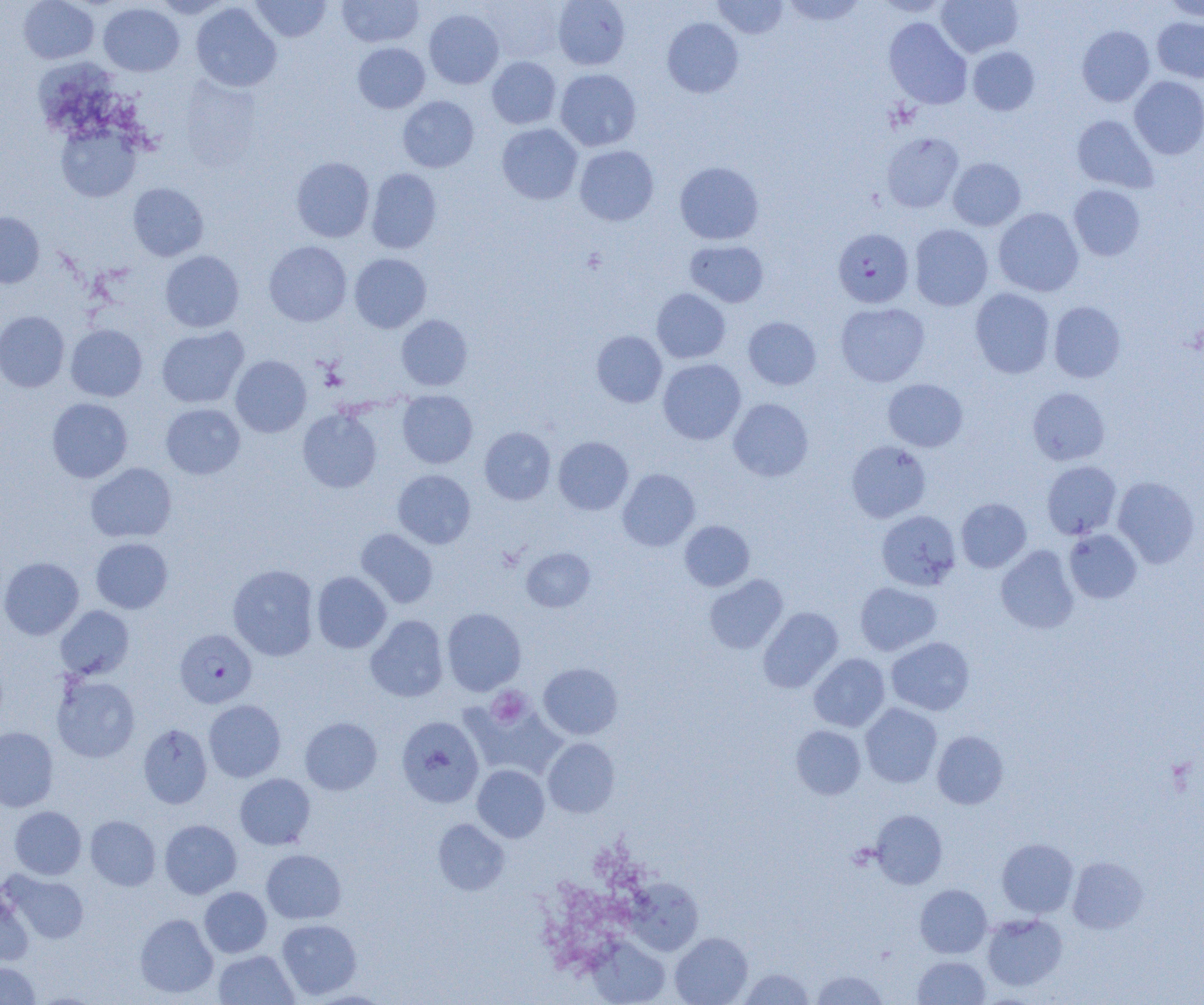

Summary:
  - Coordinate format: approximate bounding boxes as named x1/y1/x2/y2 corners in pixels
  - Platelet locations: (x1=487, y1=686, x2=531, y2=728)
  - Uninfected red blood cell locations: (x1=18, y1=0, x2=98, y2=63), (x1=152, y1=0, x2=231, y2=18), (x1=251, y1=0, x2=331, y2=42), (x1=337, y1=0, x2=424, y2=47), (x1=478, y1=0, x2=565, y2=64), (x1=553, y1=0, x2=630, y2=70), (x1=712, y1=0, x2=788, y2=39), (x1=779, y1=0, x2=868, y2=27), (x1=872, y1=0, x2=953, y2=18), (x1=936, y1=0, x2=1023, y2=57), (x1=1161, y1=0, x2=1204, y2=21), (x1=191, y1=2, x2=281, y2=92), (x1=99, y1=3, x2=184, y2=76), (x1=424, y1=9, x2=504, y2=89), (x1=1152, y1=16, x2=1204, y2=82), (x1=662, y1=17, x2=744, y2=98), (x1=884, y1=17, x2=972, y2=109), (x1=1077, y1=25, x2=1155, y2=107), (x1=353, y1=42, x2=430, y2=113), (x1=967, y1=46, x2=1040, y2=115), (x1=33, y1=56, x2=119, y2=132), (x1=487, y1=56, x2=561, y2=129), (x1=555, y1=69, x2=641, y2=151), (x1=1129, y1=76, x2=1204, y2=159), (x1=178, y1=77, x2=263, y2=172), (x1=398, y1=96, x2=479, y2=172), (x1=1071, y1=115, x2=1159, y2=193), (x1=496, y1=123, x2=583, y2=204), (x1=57, y1=125, x2=140, y2=202), (x1=881, y1=132, x2=964, y2=213), (x1=574, y1=145, x2=659, y2=226), (x1=291, y1=157, x2=374, y2=242), (x1=948, y1=158, x2=1025, y2=230), (x1=674, y1=161, x2=764, y2=245), (x1=366, y1=168, x2=441, y2=254), (x1=127, y1=182, x2=209, y2=261), (x1=1068, y1=184, x2=1146, y2=261), (x1=993, y1=207, x2=1083, y2=296), (x1=0, y1=212, x2=44, y2=288), (x1=909, y1=224, x2=993, y2=311), (x1=685, y1=240, x2=769, y2=307), (x1=264, y1=241, x2=352, y2=327), (x1=160, y1=250, x2=244, y2=332), (x1=349, y1=253, x2=431, y2=332), (x1=652, y1=288, x2=731, y2=364), (x1=970, y1=288, x2=1055, y2=378), (x1=1048, y1=301, x2=1125, y2=383), (x1=835, y1=302, x2=930, y2=387), (x1=0, y1=311, x2=69, y2=392), (x1=396, y1=314, x2=473, y2=390), (x1=743, y1=316, x2=821, y2=390), (x1=66, y1=324, x2=147, y2=401), (x1=156, y1=326, x2=248, y2=408), (x1=591, y1=331, x2=667, y2=407), (x1=231, y1=355, x2=312, y2=437), (x1=658, y1=358, x2=746, y2=444), (x1=883, y1=379, x2=968, y2=451), (x1=1028, y1=387, x2=1110, y2=465), (x1=397, y1=390, x2=477, y2=468), (x1=47, y1=398, x2=132, y2=483), (x1=728, y1=398, x2=813, y2=481), (x1=161, y1=403, x2=245, y2=479), (x1=298, y1=408, x2=382, y2=493), (x1=479, y1=426, x2=556, y2=504), (x1=553, y1=436, x2=633, y2=514), (x1=846, y1=440, x2=931, y2=522), (x1=1042, y1=460, x2=1121, y2=539), (x1=85, y1=462, x2=176, y2=543), (x1=618, y1=468, x2=700, y2=551), (x1=393, y1=469, x2=476, y2=548), (x1=1113, y1=476, x2=1200, y2=568), (x1=956, y1=498, x2=1031, y2=572), (x1=876, y1=510, x2=961, y2=590), (x1=679, y1=520, x2=755, y2=591), (x1=356, y1=528, x2=438, y2=608), (x1=1064, y1=529, x2=1142, y2=603), (x1=91, y1=538, x2=173, y2=613), (x1=996, y1=545, x2=1079, y2=634), (x1=521, y1=547, x2=595, y2=612), (x1=0, y1=556, x2=84, y2=640), (x1=228, y1=564, x2=319, y2=661), (x1=312, y1=571, x2=392, y2=653), (x1=704, y1=574, x2=788, y2=654), (x1=855, y1=581, x2=942, y2=656), (x1=55, y1=605, x2=134, y2=680), (x1=442, y1=607, x2=526, y2=695), (x1=758, y1=607, x2=843, y2=693), (x1=365, y1=615, x2=449, y2=702), (x1=887, y1=637, x2=974, y2=715), (x1=809, y1=653, x2=890, y2=732), (x1=538, y1=663, x2=622, y2=740), (x1=52, y1=675, x2=140, y2=763), (x1=463, y1=698, x2=566, y2=780), (x1=204, y1=700, x2=286, y2=782), (x1=861, y1=704, x2=942, y2=788), (x1=396, y1=716, x2=484, y2=808), (x1=300, y1=717, x2=382, y2=795), (x1=138, y1=723, x2=212, y2=808), (x1=790, y1=725, x2=866, y2=799), (x1=0, y1=726, x2=58, y2=812), (x1=932, y1=731, x2=1008, y2=809), (x1=543, y1=738, x2=620, y2=817), (x1=472, y1=765, x2=549, y2=842), (x1=235, y1=773, x2=315, y2=849), (x1=9, y1=806, x2=86, y2=879), (x1=871, y1=810, x2=947, y2=889), (x1=85, y1=815, x2=160, y2=890), (x1=433, y1=818, x2=510, y2=896), (x1=160, y1=820, x2=241, y2=898), (x1=997, y1=838, x2=1078, y2=918), (x1=261, y1=849, x2=346, y2=923), (x1=1068, y1=856, x2=1148, y2=933), (x1=4, y1=871, x2=88, y2=944), (x1=915, y1=884, x2=992, y2=957), (x1=199, y1=887, x2=272, y2=957), (x1=0, y1=888, x2=33, y2=966), (x1=135, y1=913, x2=218, y2=998), (x1=982, y1=913, x2=1067, y2=990), (x1=277, y1=919, x2=361, y2=999), (x1=670, y1=932, x2=752, y2=1005), (x1=587, y1=935, x2=670, y2=1005), (x1=213, y1=950, x2=299, y2=1004), (x1=912, y1=955, x2=991, y2=1005), (x1=0, y1=962, x2=41, y2=1004), (x1=738, y1=968, x2=815, y2=1004), (x1=811, y1=970, x2=888, y2=1004)
  - Plasmodium falciparum-infected red blood cell locations: (x1=833, y1=228, x2=914, y2=308), (x1=175, y1=629, x2=257, y2=707)
  - Slide-level diagnosis: Plasmodium falciparum
  - Modality: light microscopy
  - Preparation: thin blood film
  - Image size: 1204×1005 pixels
  - Magnification: 1000x
  - Field of view: single